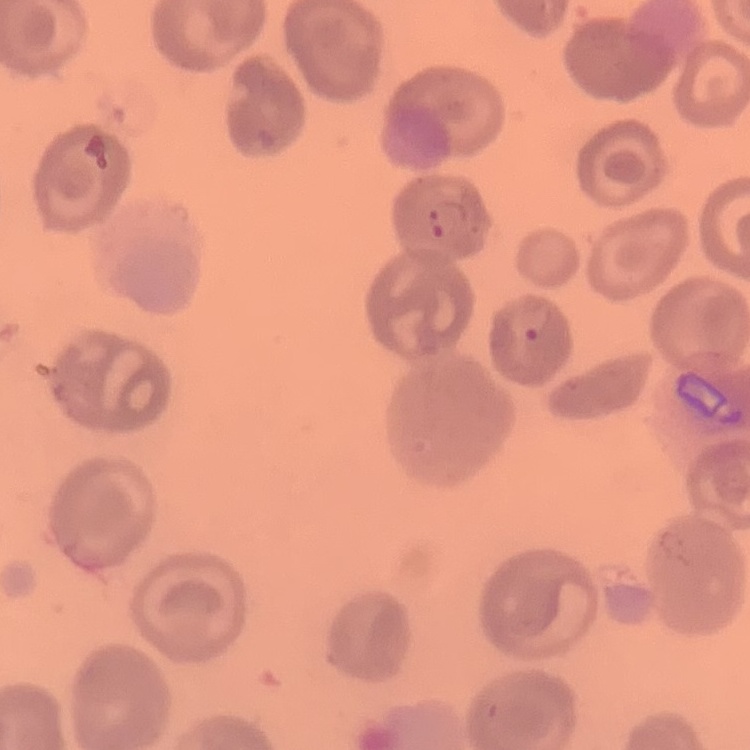

{
  "red_blood_cell_morphology": "no rouleaux formation",
  "stain": "Field's or Giemsa",
  "preparation": "thin blood film",
  "image_type": "one tile cut from a larger photomicrograph"
}